Report the malaria status of this cell.
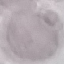

It is uninfected.

Summary:
  - Preparation: thin smear
  - Capture: smartphone through the microscope eyepiece
  - Image type: cell patch, automatically extracted from a larger field of view and resized to 64 × 64 pixels
  - Stain: Giemsa